Classify this cell by malaria status.
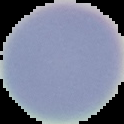

It is uninfected.

From a thin blood film. The area outside the segmented cell region is set to black. Image is 124×124 pixels.